Report the malaria status of this cell.
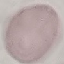

It is uninfected.

{
  "preparation": "thin smear",
  "capture": "smartphone through the microscope eyepiece",
  "stain": "Giemsa",
  "image_type": "automatically extracted cell patch, resized to 64 × 64 pixels"
}